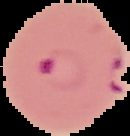
Segmented cell region on a black background. Malaria status: parasitized. From a thin blood film. Image is 130×136 pixels.